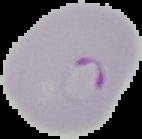

Summary:
  - Image type: segmented cell region on a black background
  - Image size: 142×139 pixels
  - Preparation: thin blood smear
  - Malaria status: parasitized